Locate every malaria parasite.
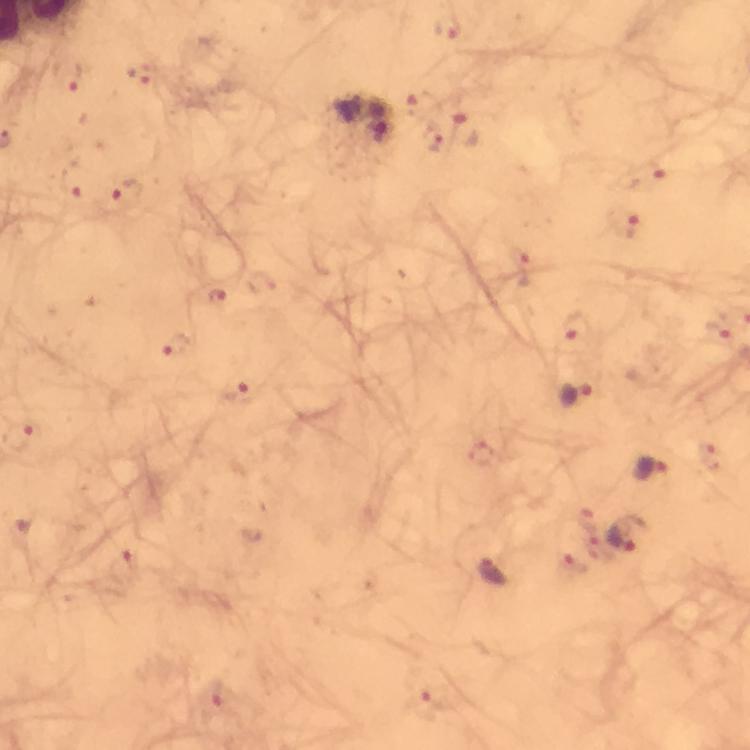
Approximate centers as (x, y) in pixels.
Malaria parasites: (452, 28), (68, 76), (144, 77), (423, 106), (470, 131), (382, 134), (437, 138), (646, 170), (73, 181), (122, 197), (625, 221), (518, 259), (219, 297), (577, 329), (716, 332), (176, 344), (242, 393), (578, 395), (482, 457), (711, 462), (651, 470), (629, 534), (125, 569), (493, 569), (214, 696), (425, 706).

Thick smear. Smartphone photograph taken through a microscope. Giemsa-stained preparation. Image is 750×750 pixels. From a diagnostic examination for malaria. Immersion oil applied. A crop from one field of view. 100x magnification.